State which parasite is depicted.
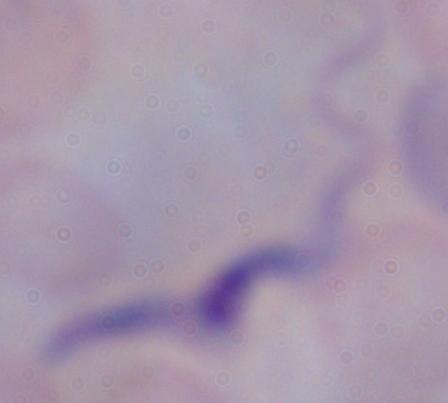
A trypanosome.

Micrograph. Captured at 1000x magnification.